Assess this cell for malaria.
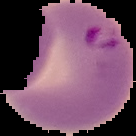

It is parasitized.

preparation = thin blood film
image size = 136×136 pixels
image type = segmented cell region on a black background